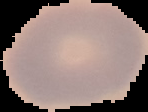

Summary:
  - Image type: segmented cell region on a black background
  - Image size: 148×112 pixels
  - Preparation: thin blood film
  - Result: negative for malaria parasites